Describe the morphology of the red blood cells.
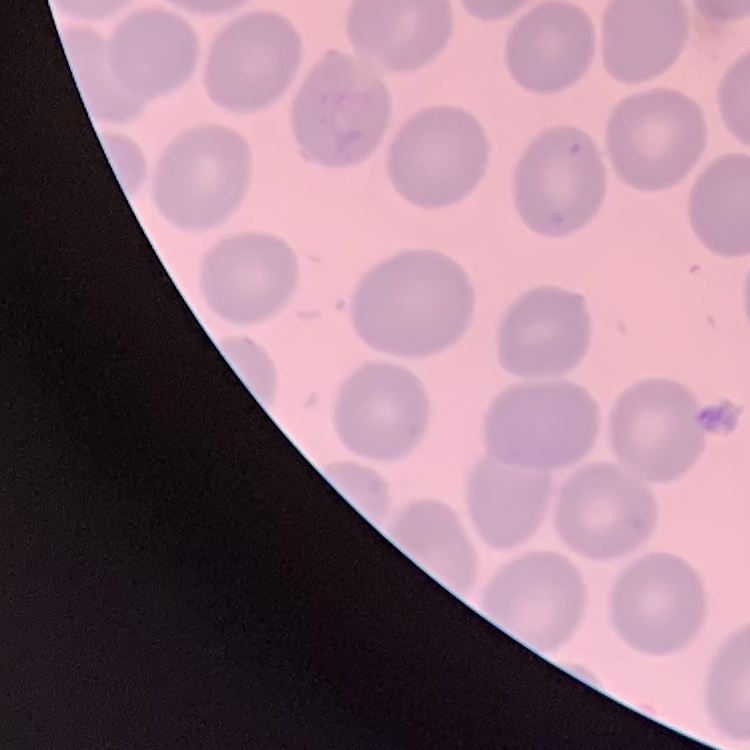
They show no rouleaux formation.

Summary:
  - Image type: square crop of a larger photomicrograph
  - Stain: Field's or Giemsa
  - Preparation: thin blood film